Assess this cell for malaria.
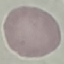

It is uninfected.

Summary:
  - Image type: automatically extracted cell patch, resized to 64 × 64 pixels
  - Preparation: thin smear
  - Stain: Giemsa
  - Capture: smartphone camera at the microscope eyepiece